Identify the parasite.
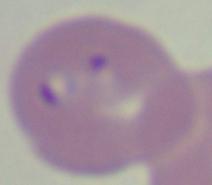
This is Babesia.

Summary:
  - Modality: micrograph
  - Magnification: 1000x